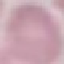
Malaria status: uninfected. Thin blood smear. Automatically extracted cell patch, resized to 64 × 64 pixels. Photographed with a smartphone camera at the microscope eyepiece. Giemsa stain.